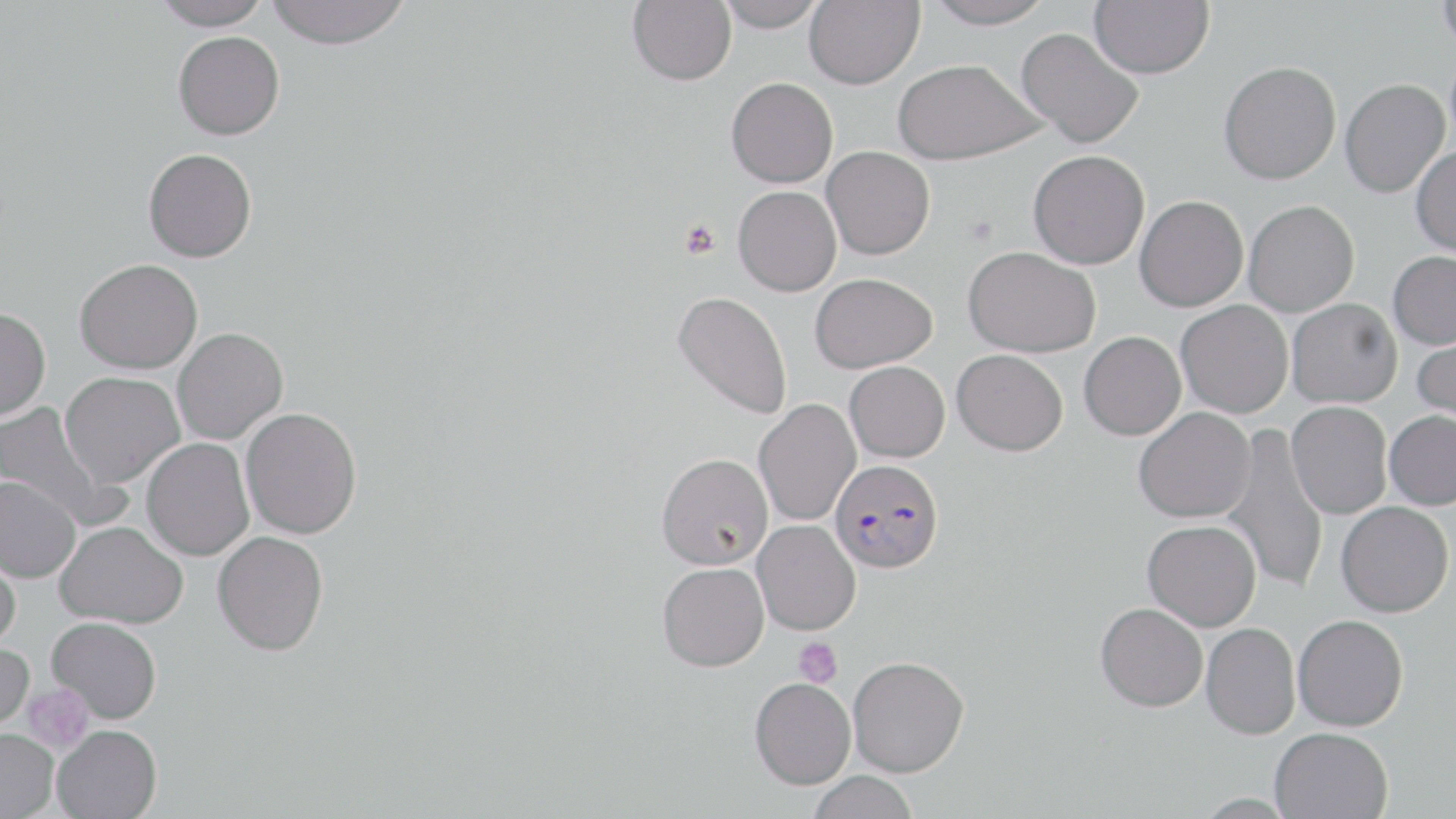

slide-level diagnosis = Plasmodium falciparum
magnification = 1000x
Plasmodium falciparum-infected red blood cell locations = approximate bounding boxes as named x1/y1/x2/y2 corners in pixels: (x1=829, y1=459, x2=943, y2=573)
modality = optical microscopy
stain = May-Grünwald-Giemsa
uninfected red blood cell locations = approximate bounding boxes as named x1/y1/x2/y2 corners in pixels: (x1=150, y1=0, x2=274, y2=30), (x1=264, y1=0, x2=412, y2=50), (x1=627, y1=0, x2=736, y2=85), (x1=715, y1=0, x2=825, y2=31), (x1=805, y1=0, x2=925, y2=89), (x1=923, y1=0, x2=1055, y2=29), (x1=1089, y1=0, x2=1214, y2=79), (x1=1437, y1=0, x2=1456, y2=54), (x1=1015, y1=27, x2=1145, y2=148), (x1=172, y1=30, x2=285, y2=140), (x1=892, y1=58, x2=1046, y2=165), (x1=1218, y1=60, x2=1341, y2=185), (x1=726, y1=77, x2=838, y2=188), (x1=1340, y1=78, x2=1450, y2=198), (x1=821, y1=146, x2=935, y2=260), (x1=1411, y1=146, x2=1456, y2=257), (x1=143, y1=148, x2=257, y2=262), (x1=1028, y1=150, x2=1149, y2=269), (x1=733, y1=186, x2=842, y2=296), (x1=1135, y1=195, x2=1249, y2=311), (x1=1244, y1=199, x2=1360, y2=316), (x1=963, y1=245, x2=1102, y2=357), (x1=1388, y1=250, x2=1456, y2=349), (x1=74, y1=258, x2=203, y2=374), (x1=810, y1=272, x2=937, y2=373), (x1=672, y1=290, x2=792, y2=420), (x1=1287, y1=298, x2=1402, y2=408), (x1=1176, y1=300, x2=1293, y2=418), (x1=0, y1=307, x2=50, y2=422), (x1=171, y1=327, x2=288, y2=445), (x1=1412, y1=329, x2=1456, y2=428), (x1=1079, y1=331, x2=1186, y2=440), (x1=952, y1=349, x2=1068, y2=456), (x1=844, y1=361, x2=950, y2=462), (x1=59, y1=371, x2=185, y2=488), (x1=754, y1=399, x2=860, y2=527), (x1=1287, y1=401, x2=1392, y2=518), (x1=0, y1=402, x2=120, y2=529), (x1=240, y1=407, x2=362, y2=539), (x1=1133, y1=407, x2=1256, y2=522), (x1=1384, y1=410, x2=1456, y2=509), (x1=1220, y1=423, x2=1329, y2=595), (x1=141, y1=438, x2=254, y2=561), (x1=656, y1=452, x2=773, y2=570), (x1=0, y1=475, x2=82, y2=583), (x1=1336, y1=502, x2=1454, y2=616), (x1=752, y1=520, x2=861, y2=635), (x1=1143, y1=520, x2=1261, y2=631), (x1=54, y1=521, x2=188, y2=628), (x1=212, y1=531, x2=329, y2=655), (x1=0, y1=540, x2=22, y2=652), (x1=657, y1=562, x2=769, y2=671), (x1=1095, y1=602, x2=1208, y2=712), (x1=1293, y1=614, x2=1408, y2=731), (x1=47, y1=617, x2=161, y2=722), (x1=1201, y1=622, x2=1300, y2=739), (x1=0, y1=642, x2=34, y2=734), (x1=847, y1=655, x2=970, y2=776), (x1=749, y1=676, x2=856, y2=789), (x1=52, y1=724, x2=162, y2=819), (x1=1270, y1=727, x2=1393, y2=818), (x1=0, y1=728, x2=59, y2=818), (x1=807, y1=771, x2=919, y2=819)
preparation = thin blood smear
image size = 1456×819 pixels
platelet locations = approximate bounding boxes as named x1/y1/x2/y2 corners in pixels: (x1=679, y1=219, x2=722, y2=260), (x1=793, y1=637, x2=842, y2=686), (x1=22, y1=684, x2=94, y2=754)
field of view = single